Outline each Plasmodium falciparum-infected red blood cell.
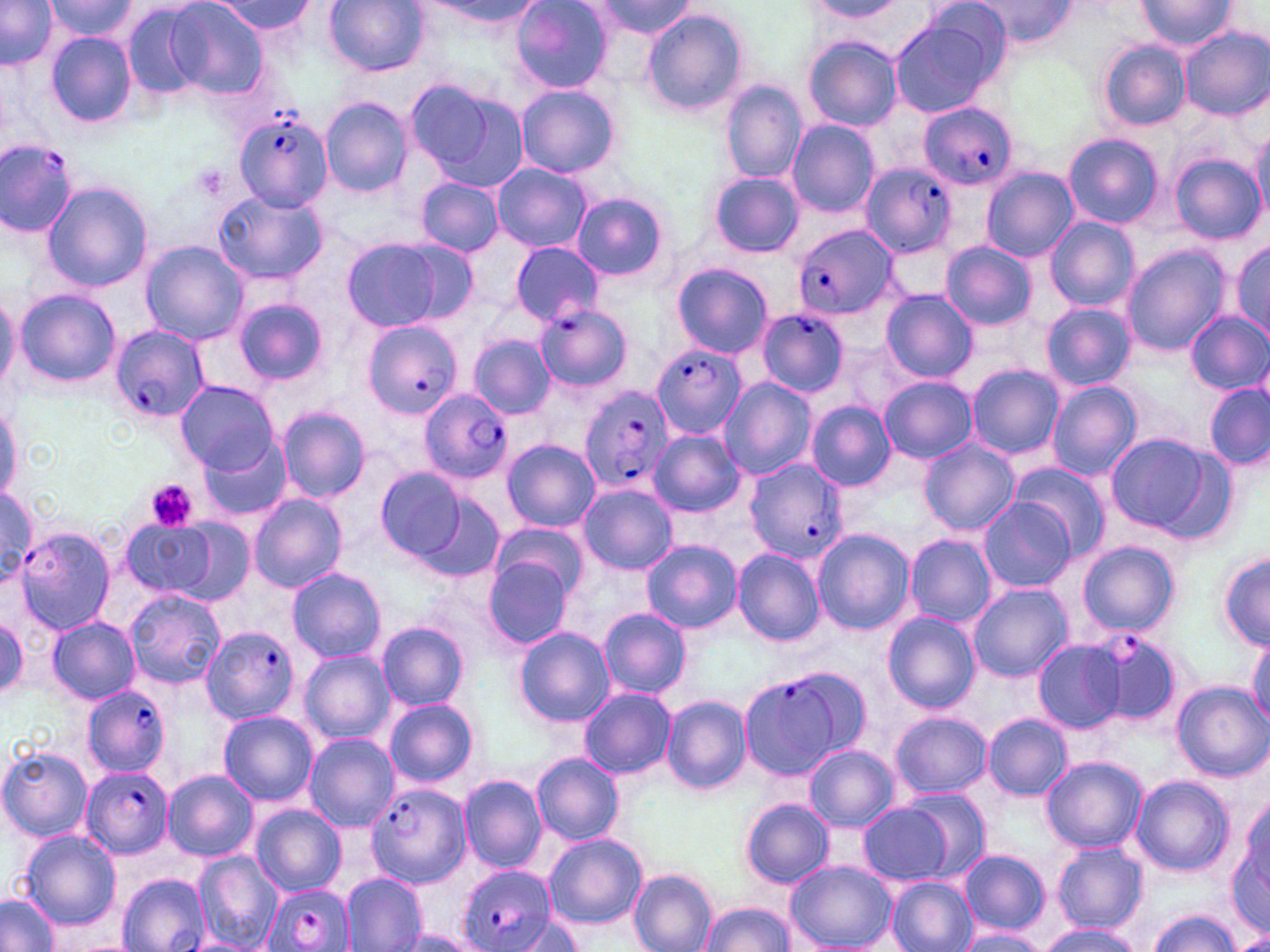

Approximate bounding boxes as (x1,y1)-(x2,y2) corner pairs in pixels.
Plasmodium falciparum-infected red blood cells: (919,101)-(1018,192), (235,111)-(336,212), (0,139)-(79,235), (862,158)-(957,259), (794,223)-(897,321), (535,301)-(634,393), (755,309)-(848,397), (362,319)-(462,421), (110,324)-(210,422), (651,344)-(745,439), (577,385)-(673,494), (419,388)-(513,484), (745,458)-(852,565), (16,526)-(117,635), (202,627)-(298,724), (1089,630)-(1186,729), (739,676)-(840,780), (78,684)-(171,777), (81,767)-(173,858), (367,782)-(471,887), (456,865)-(558,952), (264,882)-(355,952).

slide-level diagnosis = Plasmodium falciparum
image size = 1270×952 pixels
modality = light microscopy
platelet locations = approximate bounding boxes as (x1,y1)-(x2,y2) corner pairs in pixels: (147,480)-(197,532)
uninfected red blood cell locations = approximate bounding boxes as (x1,y1)-(x2,y2) corner pairs in pixels: (0,0)-(59,71), (324,0)-(429,76), (586,0)-(699,42), (1134,0)-(1239,52), (42,1)-(142,47), (211,1)-(314,35), (414,1)-(547,30), (805,1)-(905,21), (972,1)-(1079,47), (512,2)-(612,92), (163,3)-(266,99), (121,4)-(206,101), (641,10)-(748,117), (888,14)-(1001,120), (1176,26)-(1269,121), (45,30)-(138,128), (804,37)-(902,132), (1097,40)-(1191,132), (404,76)-(529,194), (721,80)-(808,184), (515,85)-(621,179), (321,96)-(414,197), (786,120)-(879,216), (1250,129)-(1269,222), (1063,133)-(1164,230), (1169,154)-(1264,243), (492,162)-(591,253), (981,168)-(1077,262), (709,171)-(803,258), (416,177)-(503,257), (42,181)-(152,292), (215,188)-(326,286), (571,192)-(669,281), (1045,217)-(1138,311), (340,238)-(464,333), (139,240)-(248,344), (1230,240)-(1269,339), (941,241)-(1036,332), (510,243)-(603,324), (1121,244)-(1230,355), (672,262)-(773,358), (0,288)-(18,391), (16,289)-(121,388), (884,289)-(976,384), (232,297)-(326,384), (1041,302)-(1135,391), (1185,310)-(1270,395), (469,333)-(555,419), (966,364)-(1064,460), (880,377)-(978,462), (718,378)-(816,479), (175,381)-(278,473), (1047,381)-(1142,480), (1205,381)-(1270,471), (0,399)-(22,505), (806,402)-(896,490), (278,407)-(371,503), (649,431)-(746,518), (1103,433)-(1219,533), (201,436)-(292,521), (503,439)-(600,532), (919,439)-(1019,536), (1011,462)-(1110,560), (378,467)-(470,562), (578,483)-(677,575), (1,487)-(40,583), (408,488)-(506,581), (249,493)-(346,594), (979,496)-(1075,592), (171,519)-(254,605), (123,520)-(218,597), (490,523)-(588,605), (812,528)-(915,634), (904,534)-(998,627), (642,539)-(741,633), (1075,539)-(1180,640), (734,548)-(826,645), (1219,552)-(1270,650), (483,556)-(576,650), (287,567)-(386,663), (968,584)-(1073,683), (125,591)-(224,690), (599,607)-(691,700), (883,612)-(979,713), (0,616)-(26,697), (47,617)-(138,703), (377,622)-(469,710), (515,627)-(614,726), (1247,632)-(1270,728), (1032,639)-(1126,732), (298,650)-(394,743), (781,664)-(873,761), (1172,682)-(1269,782), (579,687)-(674,779), (660,695)-(751,794), (384,697)-(478,787), (218,711)-(318,805), (890,712)-(991,798), (983,714)-(1072,799), (304,733)-(399,832), (803,745)-(899,833), (0,747)-(92,842), (532,752)-(623,846), (1042,756)-(1146,852), (164,770)-(257,861), (459,775)-(545,872), (1132,776)-(1233,877), (900,789)-(991,879), (1234,797)-(1269,919), (741,799)-(834,889), (251,803)-(345,895), (857,803)-(952,885), (16,828)-(121,931), (544,833)-(647,930), (1051,843)-(1148,934), (960,850)-(1050,934), (192,851)-(282,951), (787,861)-(895,951), (628,869)-(718,952), (118,872)-(212,952), (341,872)-(427,952), (886,876)-(977,952), (0,893)-(60,951), (700,903)-(797,950), (1148,910)-(1241,952), (504,915)-(587,951), (1038,924)-(1142,952), (954,930)-(1048,952), (388,931)-(487,951), (1230,933)-(1270,952)
magnification = 1000x
stain = May-Grünwald-Giemsa
preparation = thin blood smear
field of view = single